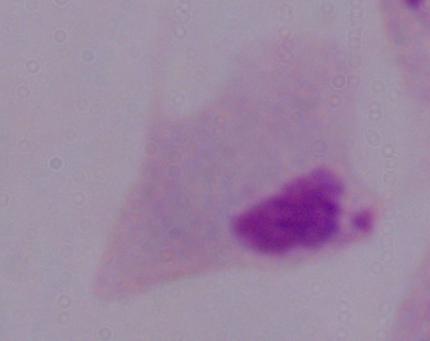 Captured at 1000x magnification. Photomicrograph. A trichomonad is shown.